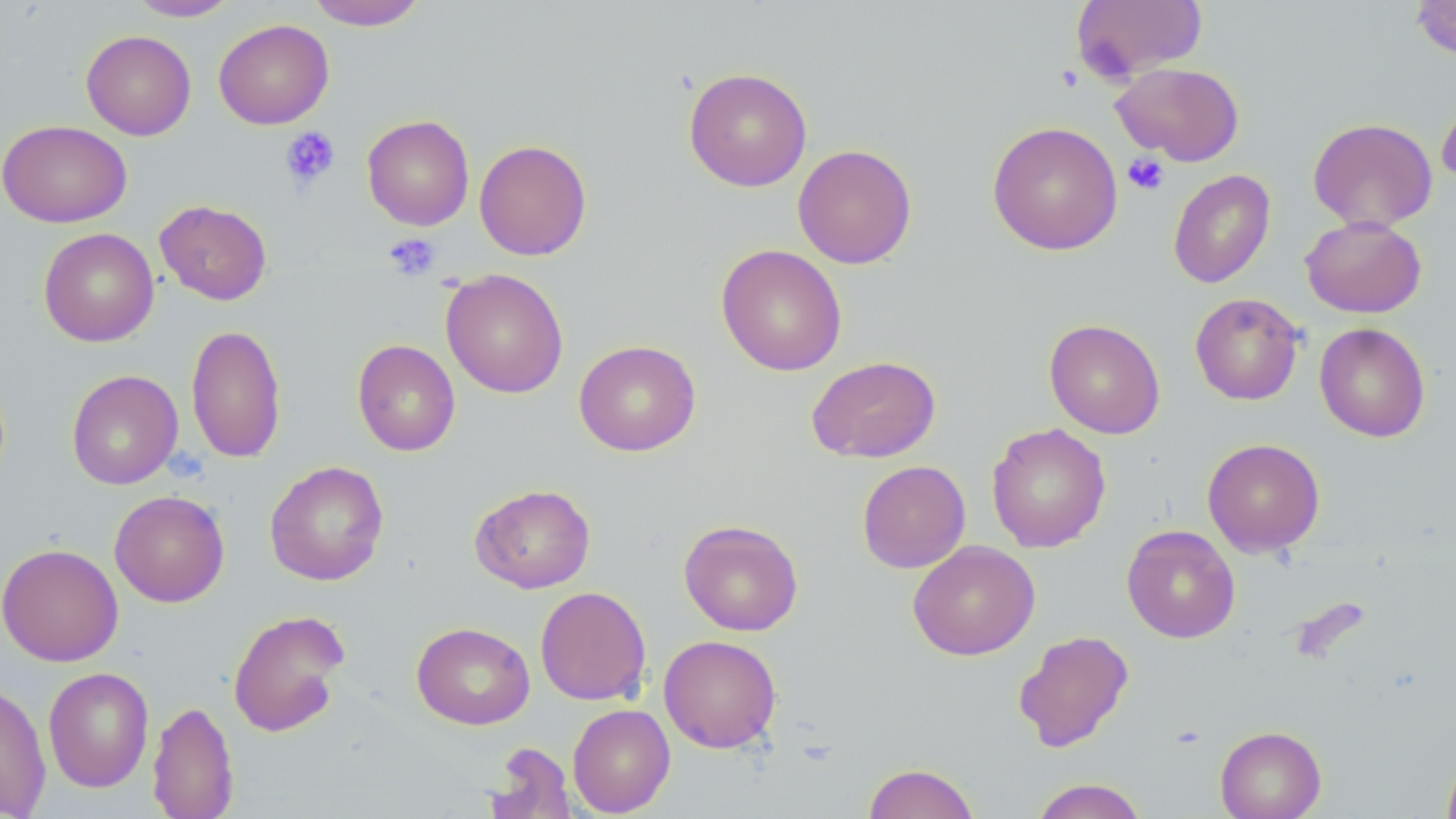

Approximate bounding boxes as (x1,y1)-(x2,y2) corner pairs in pixels. Uninfected red blood cell locations: (127,0)-(241,21), (306,0)-(429,30), (1070,0)-(1208,82), (1409,0)-(1456,61), (213,19)-(334,129), (81,30)-(196,140), (1111,62)-(1246,166), (683,67)-(812,192), (1436,93)-(1456,189), (361,114)-(475,230), (1307,117)-(1438,232), (0,119)-(133,228), (986,121)-(1123,255), (474,139)-(592,261), (792,144)-(917,269), (1167,169)-(1276,289), (155,199)-(272,305), (1300,215)-(1427,318), (38,227)-(159,347), (716,244)-(848,376), (441,268)-(568,399), (1190,292)-(1304,406), (1044,318)-(1165,439), (1314,322)-(1431,442), (186,323)-(287,463), (352,339)-(460,456), (574,339)-(701,457), (806,355)-(941,462), (66,369)-(183,490), (986,422)-(1111,553), (1203,438)-(1325,556), (264,460)-(389,586), (857,460)-(971,573), (470,484)-(596,593), (109,490)-(230,607), (678,519)-(804,636), (1121,524)-(1240,643), (907,540)-(1040,660), (0,542)-(124,666), (534,586)-(652,706), (227,608)-(350,737), (411,622)-(535,730), (1013,629)-(1134,753), (658,634)-(782,753), (43,666)-(154,793), (0,681)-(52,818), (147,699)-(239,819), (567,703)-(675,817), (1215,725)-(1326,819), (487,742)-(576,819), (1441,745)-(1456,819), (862,762)-(980,819), (1030,778)-(1147,819). Platelet locations: (1054,65)-(1084,93), (280,126)-(340,189), (1123,153)-(1170,195), (383,232)-(440,281). Slide-level diagnosis: no evidence of blood parasites. One field of a larger specimen. May-Grünwald-Giemsa-stained preparation. Image is 1456×819 pixels. Optical microscopy. Captured at 1000x magnification. Thin blood smear.